Describe the morphology of the erythrocytes.
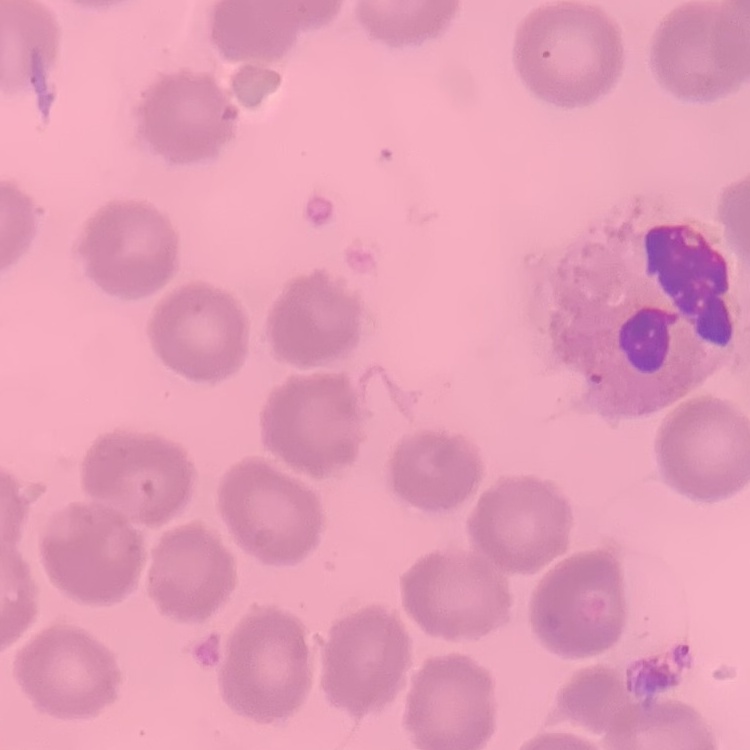

They show no rouleaux formation.

Thin peripheral smear. Stained with either Field's or Giemsa. One tile cut from a larger photomicrograph.